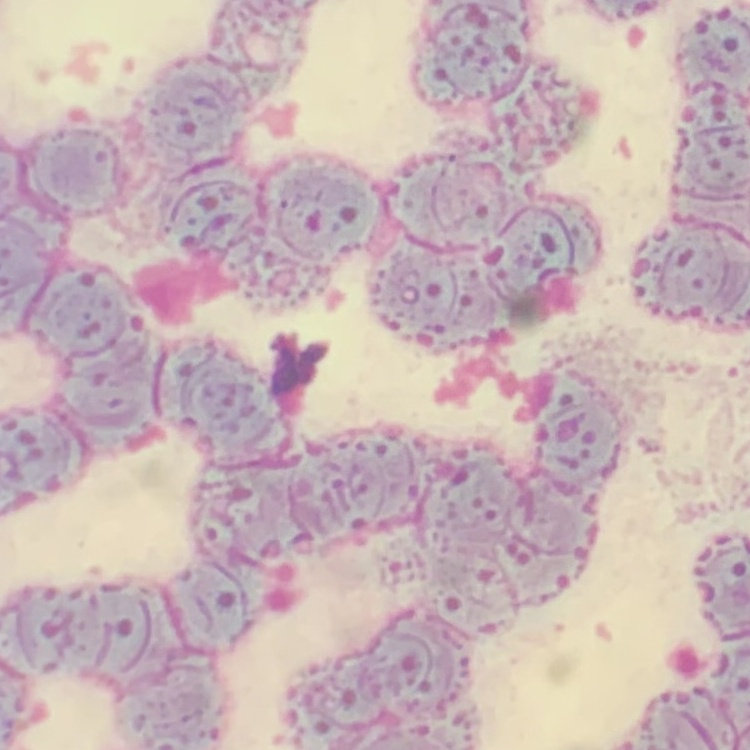
Summary:
  - Erythrocyte morphology: rouleaux formation
  - Image type: one tile cut from a larger photomicrograph
  - Stain: Field's or Giemsa
  - Preparation: thin blood smear